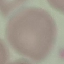

Summary:
  - Malaria status: uninfected
  - Image type: automatically extracted cell patch, resized to 64 × 64 pixels
  - Stain: Giemsa
  - Capture: smartphone camera at the microscope eyepiece
  - Preparation: thin blood film